Classify this cell by malaria status.
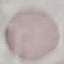

Uninfected.

Acquired by smartphone through the microscope eyepiece. Cell patch, automatically extracted from a larger field of view and resized to 64 × 64 pixels. Giemsa-stained preparation. Thin blood smear.